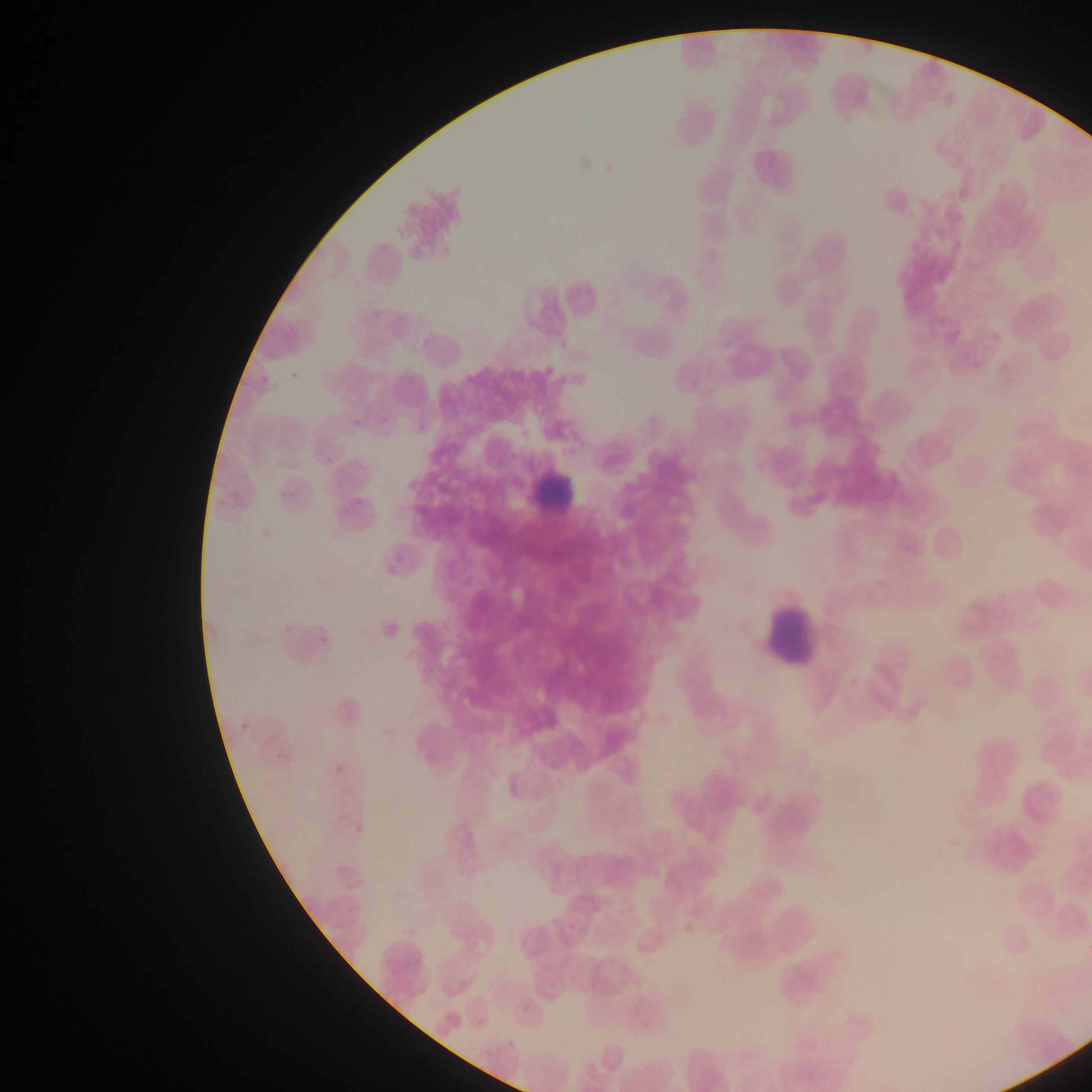

field of view = single
preparation = thin blood film
image size = 1092×1092 pixels
malaria parasite locations = approximate bounding boxes as {left, top, right, bottom} in pixels: {287, 359, 311, 383}, {254, 367, 276, 385}, {349, 413, 362, 429}, {319, 452, 336, 466}, {282, 618, 294, 637}, {317, 630, 333, 649}, {236, 716, 253, 732}, {332, 757, 346, 774}, {353, 818, 363, 833}
leukocyte locations = approximate bounding boxes as {left, top, right, bottom} in pixels: {529, 461, 582, 519}, {766, 607, 822, 665}
country = Ghana
capture = mobile-phone photograph through a microscope